Outline each blood parasite and name the species.
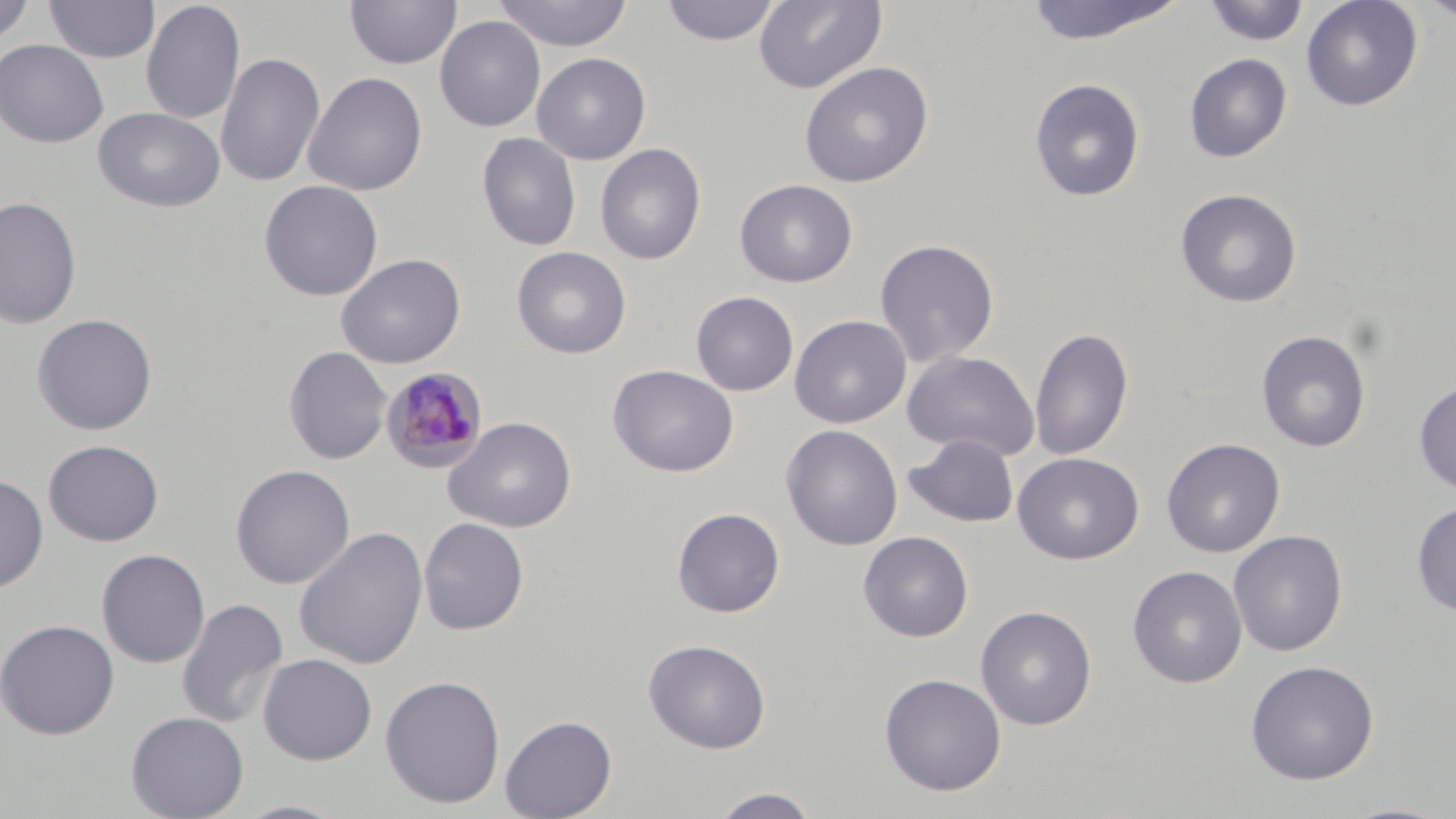

Approximate bounding boxes as [x1, y1, x2, y2] in pixels.
Plasmodium malariae-infected red blood cells: [380, 366, 488, 472].
No Plasmodium falciparum, Plasmodium ovale, Plasmodium vivax, Babesia divergens, or Trypanosoma brucei observed.

slide-level diagnosis = Plasmodium malariae
image size = 1456×819 pixels
preparation = thin blood film
modality = light microscopy
stain = May-Grünwald-Giemsa
magnification = 1000x
uninfected red blood cell locations = approximate bounding boxes as [x1, y1, x2, y2] in pixels: [0, 0, 36, 46], [43, 0, 159, 63], [345, 0, 462, 70], [493, 0, 634, 52], [659, 0, 781, 46], [753, 0, 887, 94], [1022, 0, 1188, 45], [1203, 0, 1309, 46], [1301, 0, 1422, 111], [1415, 0, 1456, 23], [140, 1, 245, 125], [434, 15, 545, 132], [0, 39, 109, 148], [215, 51, 326, 189], [531, 53, 651, 165], [1184, 53, 1293, 162], [799, 61, 934, 188], [302, 71, 427, 196], [1029, 77, 1145, 201], [92, 106, 226, 214], [477, 132, 581, 251], [595, 144, 706, 265], [735, 179, 857, 287], [258, 180, 383, 301], [1175, 188, 1302, 308], [0, 196, 82, 329], [874, 238, 999, 367], [512, 246, 631, 359], [336, 253, 465, 369], [690, 291, 798, 396], [31, 313, 157, 435], [789, 315, 911, 428], [1029, 326, 1133, 461], [1256, 329, 1371, 453], [283, 345, 391, 465], [903, 350, 1040, 461], [608, 364, 739, 477], [1414, 380, 1456, 495], [443, 416, 577, 533], [780, 424, 903, 551], [904, 434, 1019, 527], [1161, 438, 1285, 558], [43, 440, 164, 546], [1012, 452, 1144, 564], [230, 464, 355, 589], [0, 474, 49, 593], [1412, 502, 1456, 617], [672, 507, 785, 617], [418, 517, 529, 635], [293, 525, 429, 671], [1228, 530, 1348, 656], [858, 531, 973, 642], [96, 549, 210, 669], [1128, 565, 1247, 688], [175, 598, 289, 729], [975, 605, 1096, 730], [0, 618, 120, 740], [643, 638, 771, 754], [257, 653, 377, 765], [1244, 659, 1379, 785], [878, 673, 1006, 796], [379, 674, 506, 808], [125, 711, 249, 819], [500, 715, 617, 819], [708, 788, 822, 818], [232, 799, 351, 819], [1335, 801, 1454, 819]
field of view = single